Name the cell type shown.
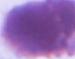

This is an erythrocyte.

Summary:
  - Magnification: 1000x
  - Modality: micrograph